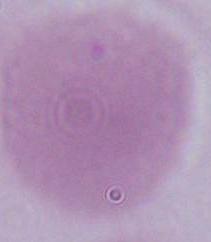
magnification = 1000x
modality = micrograph
identification = red blood cell